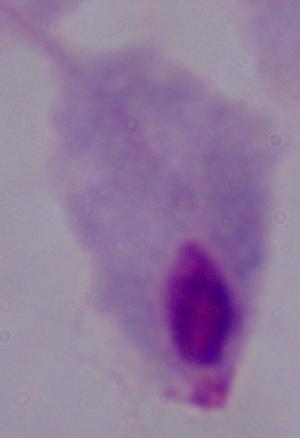

Summary:
  - Modality: micrograph
  - Magnification: 1000x
  - Identification: trichomonad